Locate every malaria parasite.
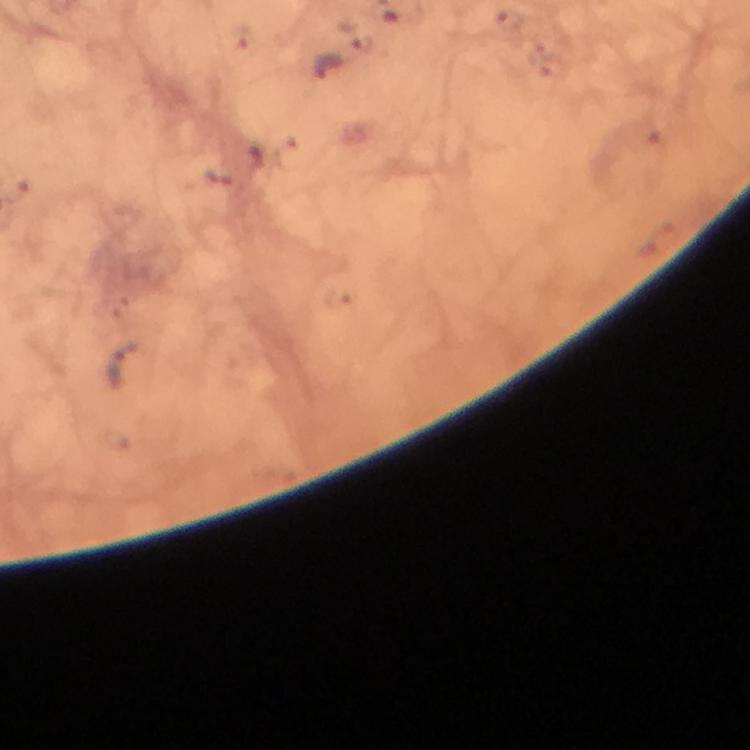
Approximate centers as [x, y] in pixels.
Malaria parasites: [328, 65], [219, 177], [122, 363].

magnification = 100x
immersion oil = used
stain = Giemsa
image size = 750×750 pixels
preparation = thick blood smear
cropped from = a single field of view
context = from a diagnostic examination for malaria
capture = smartphone photograph through a microscope